Assess the morphology of the red blood cells.
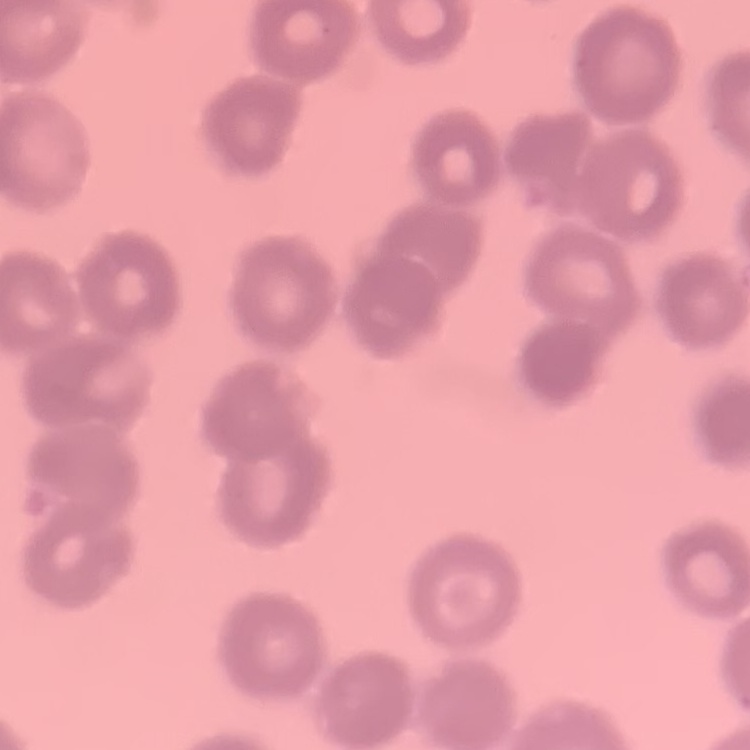

Rouleaux formation.

stain = Field's or Giemsa
preparation = thin blood smear
image type = square crop of a larger photomicrograph